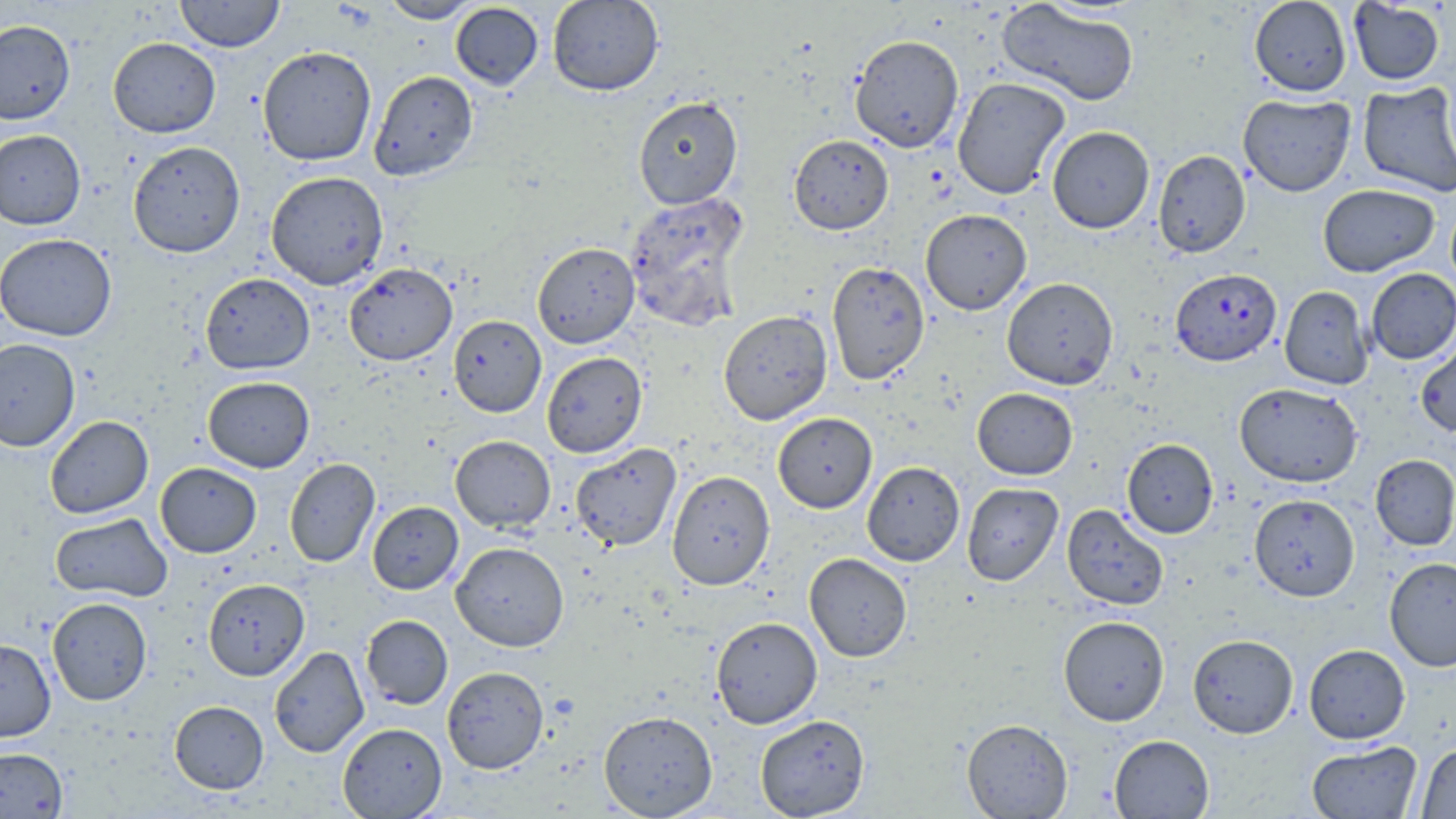
Approximate bounding boxes as (x1,y1)-(x2,y2) corner pairs in pixels. Uninfected red blood cell locations: (175,0)-(285,52), (379,0)-(483,23), (548,0)-(664,96), (1249,0)-(1352,97), (997,1)-(1139,107), (1348,1)-(1445,86), (450,2)-(544,90), (0,19)-(75,125), (849,33)-(964,152), (108,37)-(221,138), (258,46)-(377,166), (369,70)-(478,181), (952,77)-(1070,199), (1357,81)-(1456,198), (1238,93)-(1356,197), (633,95)-(743,209), (1047,126)-(1155,233), (0,130)-(85,229), (789,134)-(894,235), (128,140)-(245,257), (1153,150)-(1251,257), (266,171)-(388,290), (1318,183)-(1439,277), (623,191)-(752,332), (920,209)-(1032,315), (0,233)-(117,341), (532,242)-(640,348), (827,261)-(930,385), (344,262)-(457,365), (1366,268)-(1456,364), (200,272)-(315,374), (1002,277)-(1118,390), (1279,285)-(1373,389), (718,311)-(832,425), (448,315)-(547,417), (1416,336)-(1456,437), (0,338)-(81,451), (542,352)-(647,457), (202,376)-(315,472), (1234,382)-(1363,487), (972,387)-(1077,480), (773,413)-(877,513), (45,415)-(154,518), (450,435)-(555,533), (1122,438)-(1218,538), (570,444)-(681,551), (1370,454)-(1456,550), (284,458)-(380,568), (862,461)-(965,566), (155,462)-(262,558), (667,471)-(775,589), (962,483)-(1063,585), (1250,494)-(1360,602), (367,501)-(463,594), (1062,504)-(1169,610), (50,512)-(172,602), (451,541)-(569,651), (804,553)-(912,662), (1384,557)-(1456,672), (203,578)-(310,680), (47,597)-(152,705), (361,615)-(453,710), (711,616)-(822,729), (1058,616)-(1170,726), (1187,633)-(1298,738), (0,638)-(56,741), (1304,644)-(1410,744), (269,646)-(369,757), (442,666)-(549,774), (169,700)-(268,794), (598,710)-(718,818), (755,714)-(870,818), (961,718)-(1073,818), (337,722)-(447,818), (1109,734)-(1214,818), (1306,740)-(1422,818), (1417,743)-(1456,818), (0,746)-(68,818). Plasmodium falciparum-infected red blood cell locations: (1170,267)-(1281,367). Slide-level diagnosis: Plasmodium falciparum. May-Grünwald-Giemsa-stained preparation. Image is 1456×819 pixels. Optical microscopy. 1000x magnification. Thin blood smear. Single field of view.